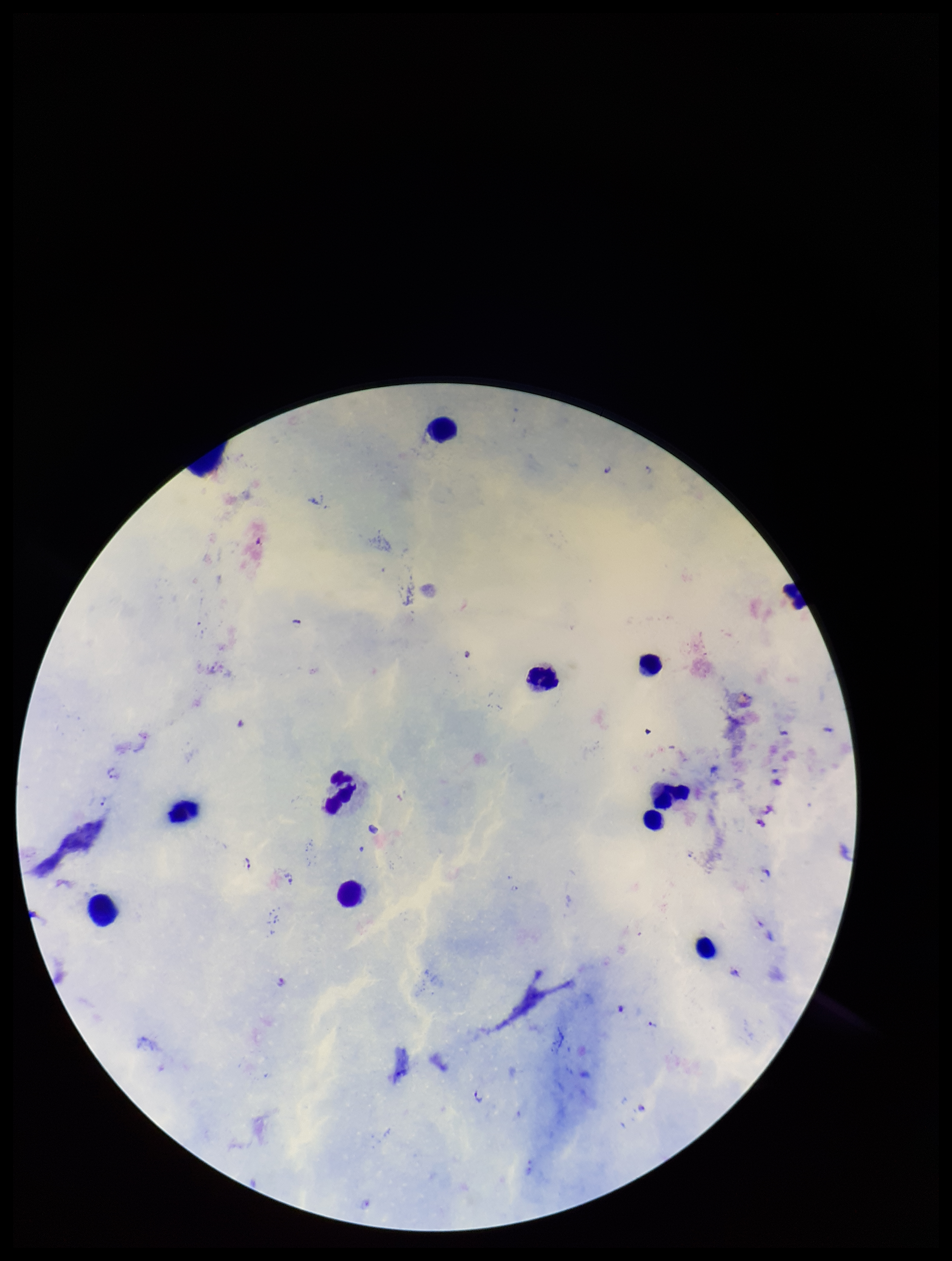 Image is 952×1261 pixels. Species reported for this patient: Plasmodium falciparum. Plasmodium parasites: detected. Leukocyte count: 12. Photographed through the microscope eyepiece with a smartphone camera. Preparation: thick blood smear. Parasite count: 5. Patient malaria status: positive. Single field of view. Giemsa stain.